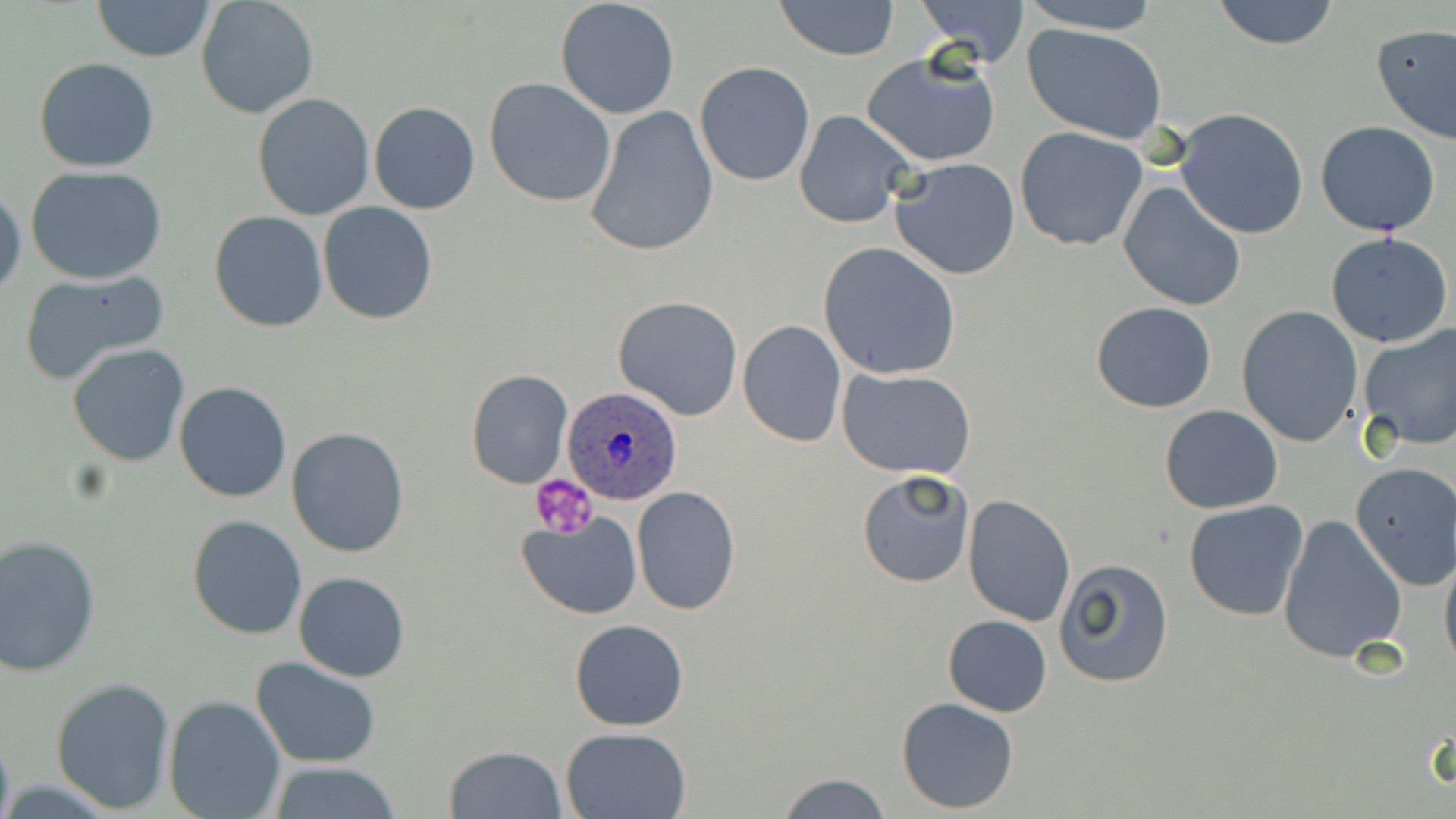

Summary:
  - Coordinate format: approximate bounding boxes as [x1, y1, x2, y2] in pixels
  - Plasmodium ovale-infected red blood cell locations: [562, 387, 683, 506]
  - Platelet locations: [530, 474, 599, 538]
  - Uninfected red blood cell locations: [91, 0, 216, 63], [195, 0, 320, 119], [553, 0, 681, 121], [773, 0, 900, 60], [913, 0, 1031, 67], [1016, 0, 1167, 33], [1208, 0, 1343, 50], [1371, 23, 1456, 145], [1022, 24, 1167, 143], [862, 52, 1004, 166], [33, 57, 160, 171], [695, 61, 815, 186], [483, 78, 617, 207], [253, 92, 375, 219], [369, 102, 479, 213], [583, 105, 719, 258], [1175, 108, 1309, 240], [795, 109, 917, 229], [1315, 120, 1441, 236], [1014, 126, 1149, 251], [889, 157, 1021, 280], [24, 164, 169, 284], [1119, 181, 1247, 313], [0, 187, 24, 299], [317, 203, 438, 323], [209, 211, 328, 332], [1325, 233, 1454, 349], [817, 242, 962, 381], [18, 268, 173, 385], [612, 296, 743, 420], [1091, 302, 1218, 412], [1235, 304, 1364, 448], [738, 320, 847, 447], [1356, 325, 1456, 453], [66, 343, 191, 467], [836, 367, 977, 480], [465, 370, 573, 489], [173, 382, 290, 502], [1159, 405, 1283, 514], [286, 426, 412, 558], [1350, 462, 1455, 589], [857, 468, 974, 589], [631, 487, 740, 614], [963, 493, 1075, 627], [1183, 499, 1308, 620], [517, 511, 642, 619], [1277, 513, 1407, 663], [187, 515, 308, 639], [0, 534, 100, 675], [1440, 547, 1456, 673], [1054, 558, 1174, 687], [293, 572, 409, 681], [943, 614, 1052, 716], [569, 619, 689, 732], [251, 657, 382, 768], [51, 677, 176, 813], [164, 696, 286, 819], [896, 698, 1020, 812], [560, 726, 693, 818], [443, 744, 567, 818], [264, 762, 407, 817], [776, 771, 892, 818]
  - Slide-level diagnosis: Plasmodium ovale
  - Stain: May-Grünwald-Giemsa
  - Magnification: 1000x
  - Preparation: thin blood smear
  - Image size: 1456×819 pixels
  - Modality: light microscopy
  - Field of view: one of a larger specimen